Assess the morphology of the erythrocytes.
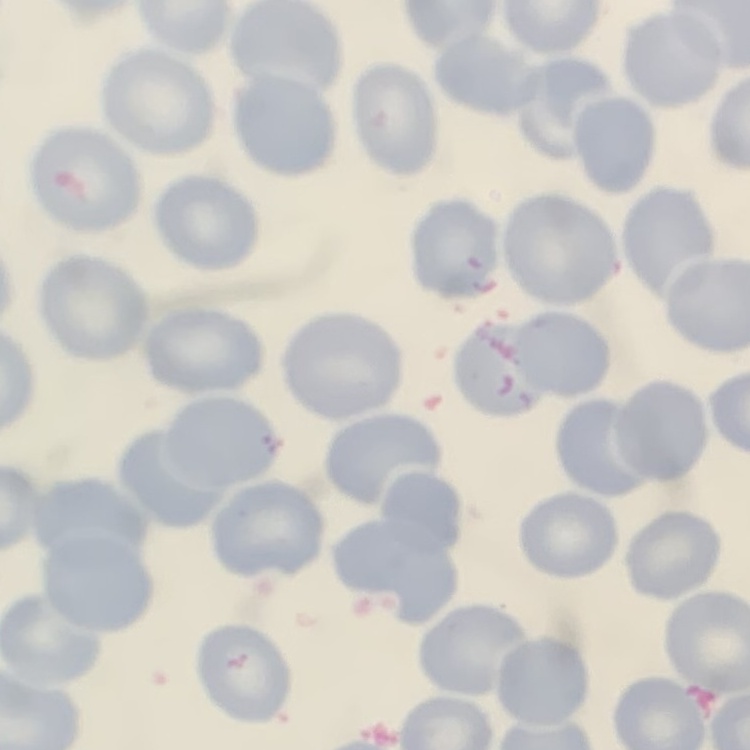

They show no rouleaux formation.

{
  "stain": "Field's or Giemsa",
  "image_type": "square crop of a larger photomicrograph",
  "preparation": "thin peripheral smear"
}